Classify this cell by malaria status.
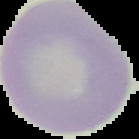

Uninfected.

The area outside the segmented cell region is set to black. Image is 139×139 pixels. From a thin blood film.